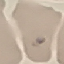

Summary:
  - Result: malaria parasites identified
  - Preparation: thin blood smear
  - Capture: smartphone camera at the microscope eyepiece
  - Stain: Giemsa
  - Image type: cell patch, automatically extracted from a larger field of view and resized to 64 × 64 pixels